Classify this cell by malaria status.
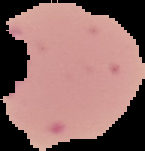

It is parasitized.

Cell region segmented out of the field of view; the surrounding area is masked to black. From a thin blood film. Image is 145×151 pixels.